Locate every blood parasite and identify its species.
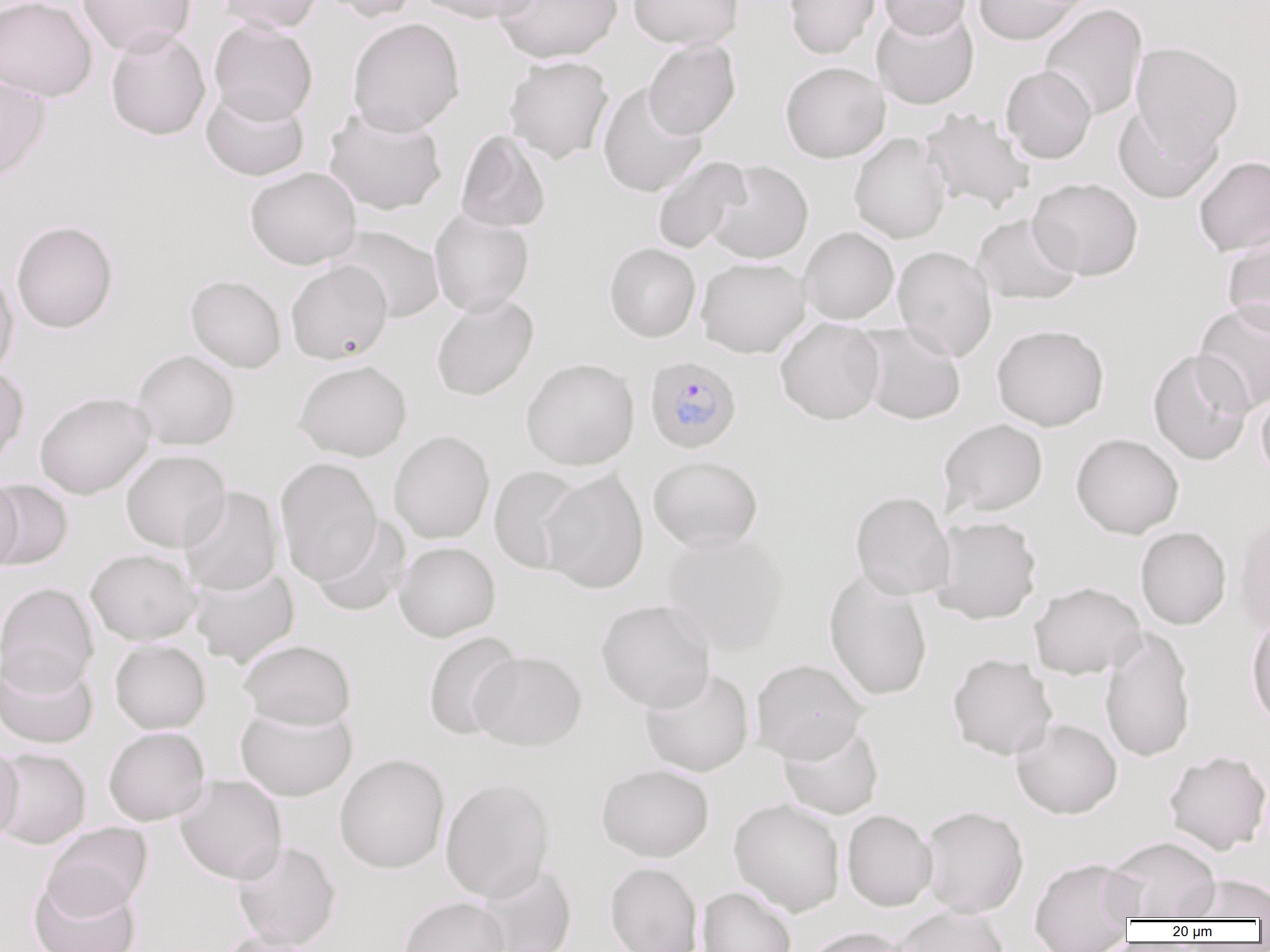
Approximate bounding boxes as named x1/y1/x2/y2 corners in pixels.
Plasmodium falciparum-infected red blood cells: (x1=643, y1=355, x2=742, y2=454).
No Plasmodium ovale, Plasmodium malariae, Plasmodium vivax, Babesia divergens, or Trypanosoma brucei observed.

Uninfected red blood cell locations: (x1=0, y1=0, x2=97, y2=101), (x1=77, y1=0, x2=196, y2=56), (x1=217, y1=0, x2=324, y2=34), (x1=318, y1=0, x2=419, y2=22), (x1=415, y1=0, x2=540, y2=24), (x1=494, y1=0, x2=622, y2=63), (x1=627, y1=0, x2=744, y2=49), (x1=784, y1=0, x2=881, y2=59), (x1=878, y1=0, x2=973, y2=39), (x1=972, y1=0, x2=1089, y2=45), (x1=1039, y1=4, x2=1147, y2=121), (x1=871, y1=8, x2=979, y2=109), (x1=347, y1=17, x2=465, y2=136), (x1=208, y1=19, x2=318, y2=124), (x1=105, y1=28, x2=211, y2=140), (x1=643, y1=38, x2=741, y2=139), (x1=1130, y1=41, x2=1244, y2=153), (x1=504, y1=56, x2=614, y2=164), (x1=780, y1=61, x2=890, y2=163), (x1=1001, y1=66, x2=1096, y2=164), (x1=0, y1=74, x2=50, y2=183), (x1=597, y1=82, x2=708, y2=198), (x1=201, y1=86, x2=310, y2=181), (x1=1113, y1=103, x2=1223, y2=203), (x1=324, y1=105, x2=448, y2=215), (x1=919, y1=108, x2=1035, y2=215), (x1=455, y1=130, x2=552, y2=233), (x1=849, y1=132, x2=951, y2=244), (x1=651, y1=156, x2=751, y2=255), (x1=1193, y1=156, x2=1270, y2=256), (x1=705, y1=160, x2=813, y2=264), (x1=244, y1=166, x2=362, y2=270), (x1=1028, y1=177, x2=1143, y2=281), (x1=429, y1=209, x2=535, y2=316), (x1=972, y1=213, x2=1082, y2=306), (x1=11, y1=220, x2=118, y2=333), (x1=330, y1=225, x2=445, y2=324), (x1=799, y1=226, x2=899, y2=325), (x1=1222, y1=233, x2=1270, y2=335), (x1=604, y1=242, x2=701, y2=342), (x1=893, y1=245, x2=997, y2=362), (x1=695, y1=257, x2=811, y2=358), (x1=286, y1=260, x2=393, y2=364), (x1=0, y1=267, x2=19, y2=380), (x1=185, y1=274, x2=287, y2=373), (x1=431, y1=294, x2=538, y2=401), (x1=1192, y1=300, x2=1270, y2=414), (x1=775, y1=318, x2=885, y2=425), (x1=853, y1=323, x2=967, y2=425), (x1=991, y1=323, x2=1109, y2=431), (x1=132, y1=349, x2=240, y2=450), (x1=1147, y1=349, x2=1253, y2=466), (x1=521, y1=358, x2=640, y2=470), (x1=294, y1=360, x2=412, y2=461), (x1=0, y1=365, x2=30, y2=469), (x1=1256, y1=391, x2=1270, y2=486), (x1=34, y1=392, x2=155, y2=499), (x1=938, y1=418, x2=1048, y2=519), (x1=389, y1=430, x2=495, y2=544), (x1=1070, y1=433, x2=1184, y2=538), (x1=121, y1=449, x2=231, y2=552), (x1=648, y1=455, x2=763, y2=551), (x1=275, y1=457, x2=382, y2=586), (x1=488, y1=466, x2=586, y2=575), (x1=540, y1=469, x2=649, y2=595), (x1=0, y1=476, x2=23, y2=573), (x1=1, y1=479, x2=73, y2=570), (x1=178, y1=486, x2=283, y2=596), (x1=850, y1=491, x2=954, y2=600), (x1=1234, y1=514, x2=1270, y2=634), (x1=309, y1=516, x2=411, y2=617), (x1=928, y1=516, x2=1042, y2=624), (x1=1135, y1=526, x2=1232, y2=629), (x1=661, y1=531, x2=787, y2=654), (x1=394, y1=541, x2=500, y2=641), (x1=85, y1=549, x2=200, y2=645), (x1=189, y1=564, x2=300, y2=666), (x1=823, y1=571, x2=933, y2=702), (x1=1029, y1=581, x2=1146, y2=680), (x1=0, y1=582, x2=99, y2=693), (x1=596, y1=599, x2=716, y2=712), (x1=1246, y1=614, x2=1270, y2=731), (x1=1100, y1=628, x2=1196, y2=763), (x1=422, y1=630, x2=522, y2=740), (x1=110, y1=639, x2=211, y2=733), (x1=239, y1=639, x2=357, y2=731), (x1=0, y1=651, x2=99, y2=749), (x1=470, y1=651, x2=587, y2=751), (x1=947, y1=653, x2=1057, y2=759), (x1=749, y1=658, x2=869, y2=763), (x1=640, y1=667, x2=755, y2=777), (x1=235, y1=703, x2=357, y2=802), (x1=1011, y1=717, x2=1122, y2=819), (x1=777, y1=721, x2=884, y2=819), (x1=103, y1=726, x2=209, y2=825), (x1=0, y1=743, x2=24, y2=846), (x1=0, y1=747, x2=91, y2=849), (x1=1163, y1=749, x2=1270, y2=855), (x1=334, y1=753, x2=450, y2=874), (x1=596, y1=763, x2=714, y2=862), (x1=174, y1=774, x2=288, y2=884), (x1=440, y1=776, x2=556, y2=902), (x1=728, y1=799, x2=846, y2=917), (x1=918, y1=805, x2=1029, y2=918), (x1=841, y1=809, x2=937, y2=911), (x1=42, y1=822, x2=152, y2=919), (x1=1104, y1=836, x2=1221, y2=921), (x1=232, y1=840, x2=341, y2=950), (x1=1029, y1=856, x2=1140, y2=952), (x1=472, y1=862, x2=578, y2=952), (x1=604, y1=862, x2=704, y2=952), (x1=1181, y1=874, x2=1270, y2=920), (x1=29, y1=875, x2=141, y2=952), (x1=697, y1=886, x2=797, y2=952), (x1=397, y1=896, x2=510, y2=952), (x1=890, y1=906, x2=1011, y2=952), (x1=800, y1=926, x2=916, y2=952), (x1=214, y1=929, x2=324, y2=952). Slide-level diagnosis: Plasmodium falciparum. Captured at 1000x magnification. Thin blood smear. One field of a larger specimen. Image is 1270×952 pixels. Optical microscopy.